Point out every Plasmodium parasite and every leukocyte.
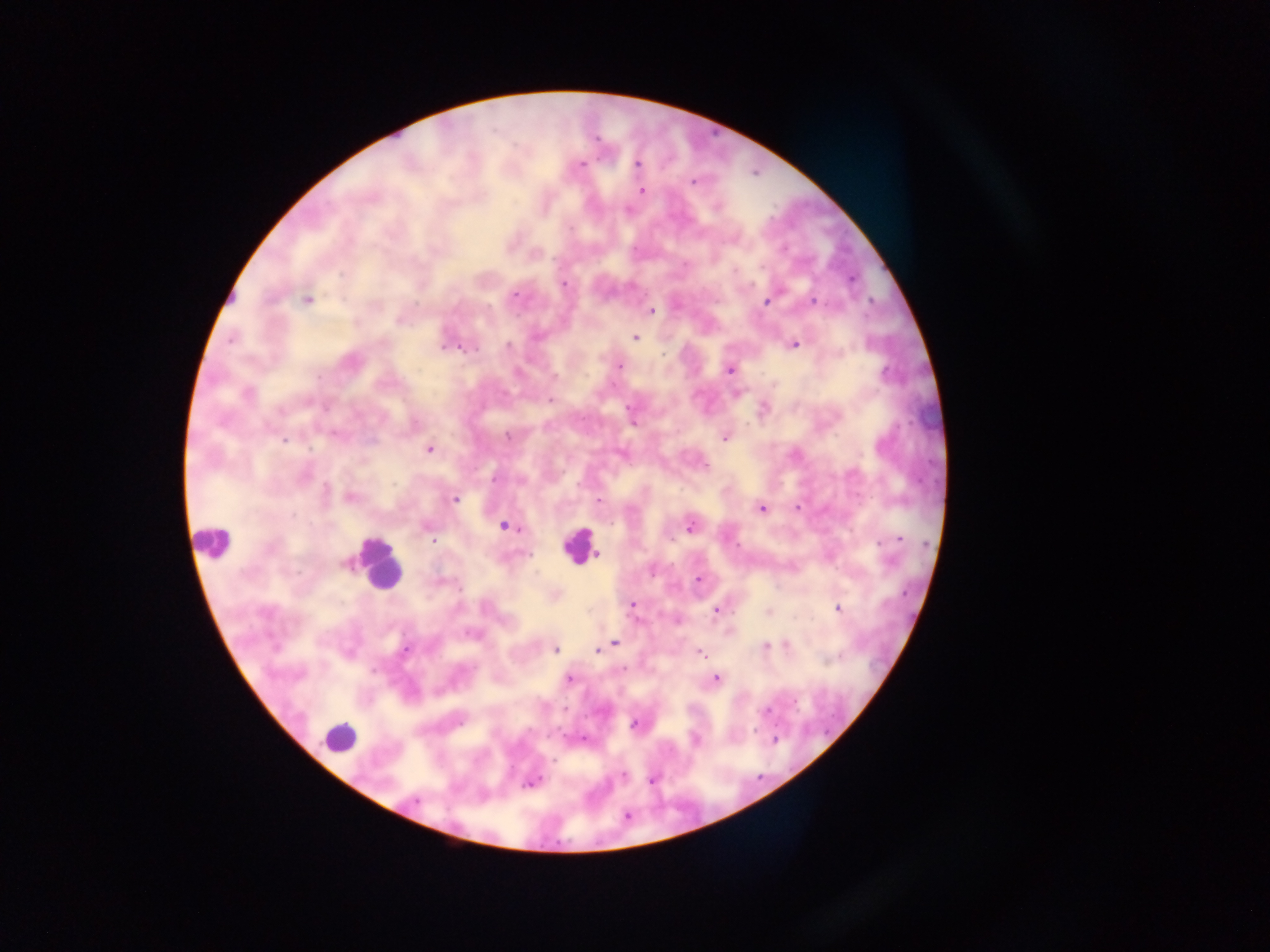
Approximate centers as (x, y) in pixels.
Plasmodium parasites: (596, 139), (581, 165), (638, 165), (693, 181), (641, 191), (716, 207), (570, 228), (734, 270), (853, 279), (564, 284), (515, 295), (307, 300), (813, 300), (765, 302), (870, 302), (652, 311), (399, 321), (636, 337), (538, 338), (231, 339), (795, 344), (508, 346), (443, 348), (450, 348), (469, 349), (663, 354), (620, 366), (729, 370), (886, 375), (555, 376), (248, 393), (550, 399), (628, 407), (281, 412), (633, 424), (508, 437), (725, 438), (285, 440), (429, 449), (705, 466), (495, 478), (326, 489), (351, 497), (455, 499), (599, 500), (797, 508), (762, 510), (505, 526), (690, 526), (898, 539), (432, 541), (881, 543), (598, 553), (529, 554), (344, 563), (698, 579), (460, 588), (633, 605), (838, 609), (716, 611), (768, 612), (472, 635), (615, 642), (787, 644), (765, 646), (406, 650), (555, 650), (598, 651), (701, 653), (838, 658), (624, 669), (373, 670), (569, 679), (716, 679), (766, 711), (633, 725), (755, 730), (584, 739), (775, 739), (695, 741), (553, 761), (623, 776), (651, 780), (532, 783), (415, 801).
Leukocytes: (212, 540), (579, 546), (379, 566), (338, 738).

Image is 1270×952 pixels. Thick blood smear. Single field of view. Photographed through a microscope with a mobile-phone camera. Sample from Ghana.